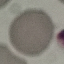

Result: negative for malaria parasites. Giemsa-stained preparation. Thin blood smear. Acquired by smartphone through the microscope eyepiece. Cell patch, automatically extracted from a larger field of view and resized to 64 × 64 pixels.